Point out each leukocyte.
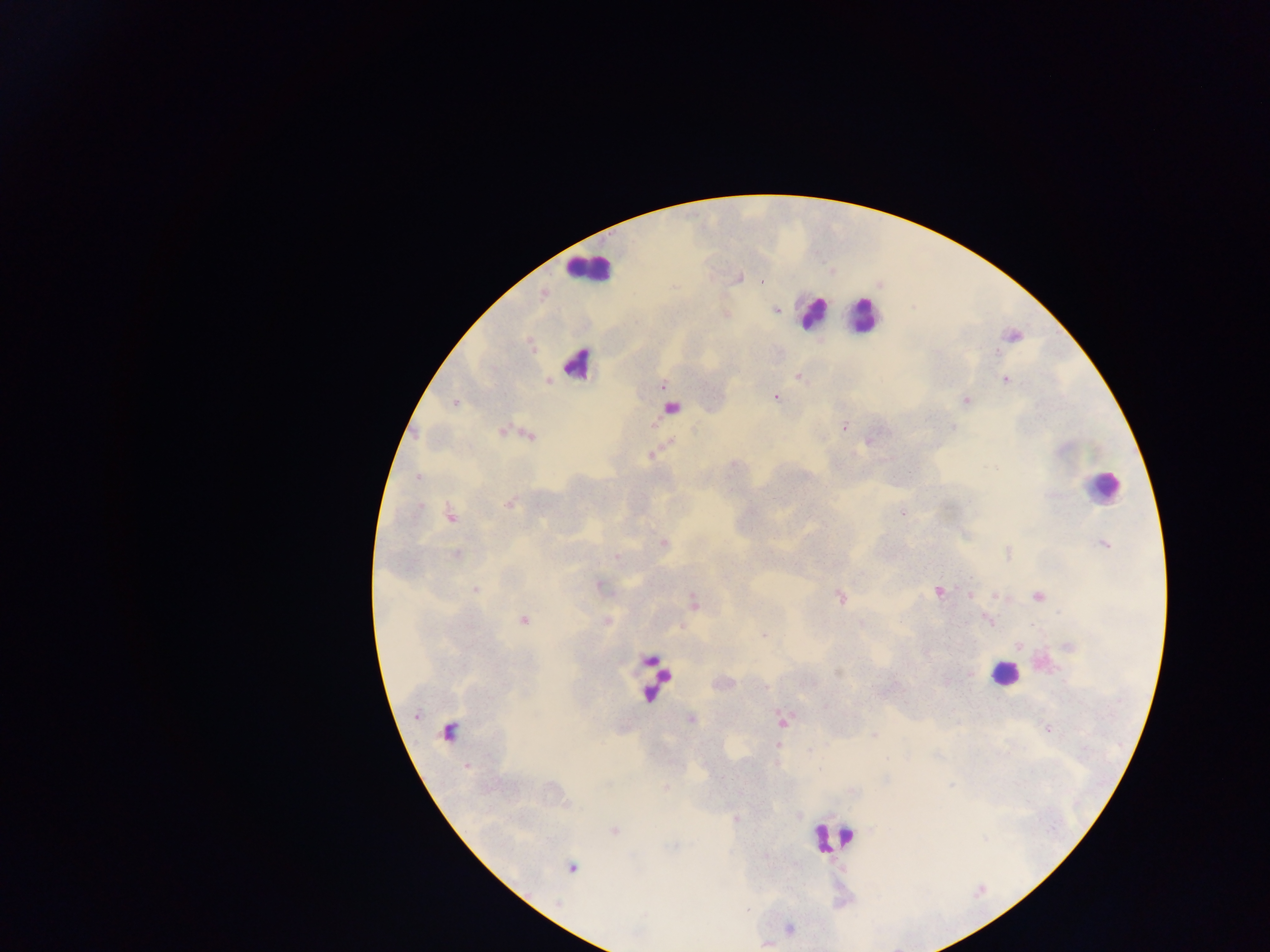
Approximate centers as {x, y} in pixels.
Leukocytes: {589, 269}, {812, 312}, {863, 315}, {576, 363}, {1103, 488}, {1004, 673}, {655, 680}, {833, 837}.

Plasmodium parasite locations: {739, 277}, {762, 281}, {776, 310}, {725, 314}, {1013, 336}, {797, 375}, {1004, 379}, {548, 380}, {662, 384}, {775, 397}, {965, 400}, {454, 402}, {670, 407}, {844, 426}, {503, 431}, {514, 432}, {529, 434}, {869, 439}, {652, 455}, {509, 503}, {901, 513}, {451, 515}, {662, 543}, {1105, 543}, {456, 554}, {598, 585}, {475, 590}, {938, 591}, {970, 595}, {839, 596}, {1037, 597}, {692, 602}, {988, 619}, {523, 620}, {606, 621}, {861, 624}, {765, 635}, {1019, 645}, {691, 719}, {782, 720}, {449, 731}, {874, 735}, {613, 830}, {571, 867}, {789, 929}, {766, 943}. Sample from Ghana. Photographed through a microscope with a mobile-phone camera. Image is 1270×952 pixels. Single field of view. Thick blood smear.